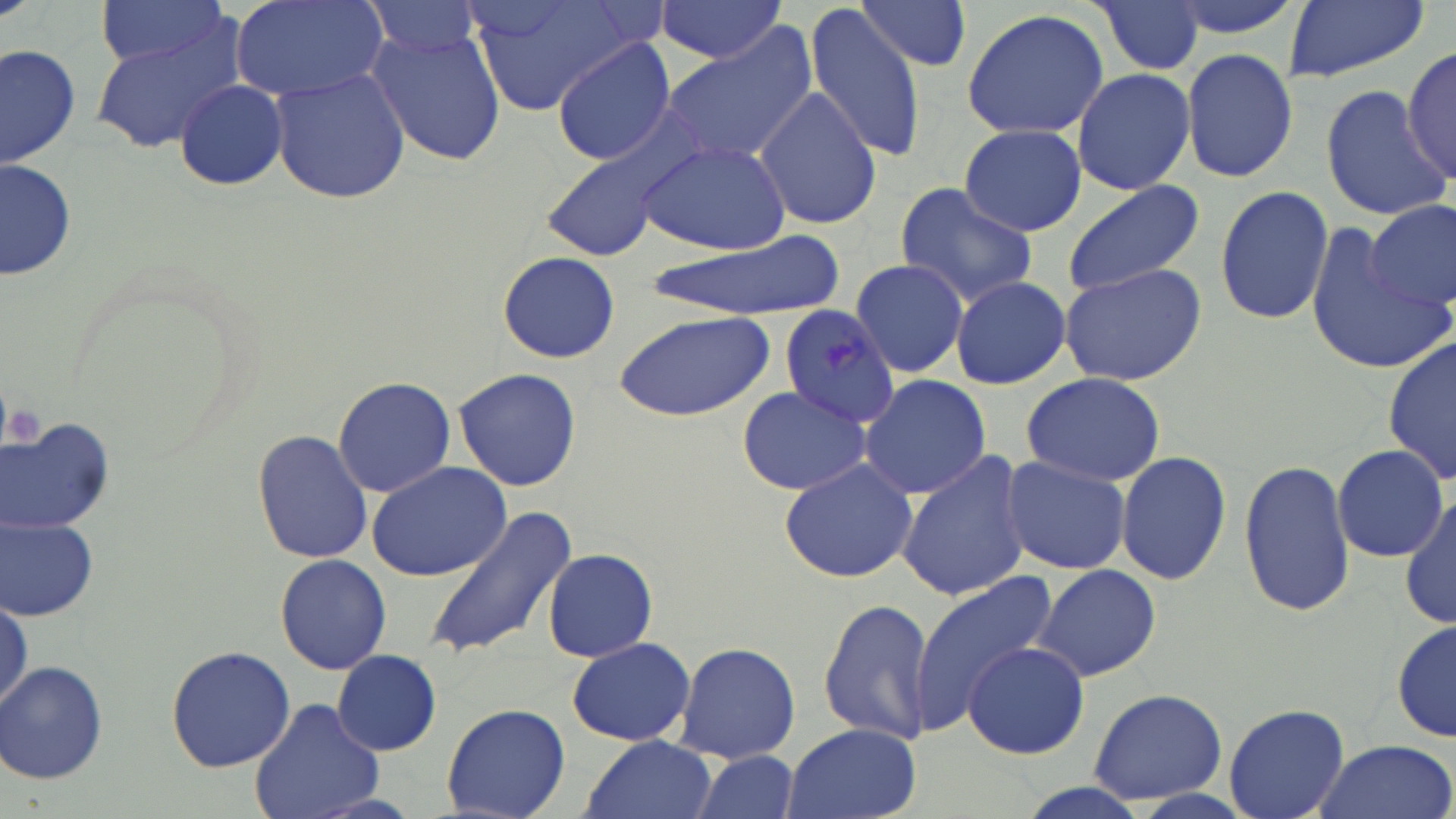 Approximate bounding boxes as (x1, y1, x2, y2) in pixels. Uninfected red blood cell locations: (95, 0, 226, 70), (360, 0, 487, 59), (473, 0, 635, 116), (652, 0, 788, 63), (856, 0, 976, 76), (1279, 0, 1429, 82), (231, 1, 385, 100), (1090, 2, 1204, 77), (804, 7, 924, 164), (958, 8, 1111, 140), (366, 24, 508, 167), (92, 28, 240, 151), (656, 28, 817, 170), (551, 40, 676, 167), (2, 42, 81, 169), (1403, 45, 1456, 187), (1180, 48, 1299, 183), (270, 66, 409, 205), (1071, 66, 1196, 196), (172, 79, 289, 191), (1319, 84, 1448, 221), (753, 85, 881, 233), (959, 123, 1087, 237), (535, 129, 697, 266), (638, 140, 791, 255), (1, 156, 77, 282), (1060, 180, 1205, 296), (894, 182, 1040, 308), (1214, 183, 1334, 327), (1369, 204, 1455, 311), (1303, 223, 1449, 375), (647, 235, 844, 320), (496, 251, 621, 364), (849, 257, 972, 380), (1058, 263, 1207, 387), (949, 275, 1070, 389), (612, 309, 775, 421), (1384, 336, 1456, 487), (452, 368, 585, 494), (1021, 371, 1168, 488), (859, 373, 992, 500), (332, 376, 456, 499), (736, 384, 877, 496), (1, 417, 120, 532), (253, 428, 373, 565), (1333, 444, 1448, 563), (1116, 450, 1233, 585), (895, 452, 1032, 603), (1000, 454, 1132, 574), (778, 458, 919, 583), (1240, 458, 1355, 618), (367, 461, 515, 582), (1400, 491, 1456, 634), (422, 504, 578, 662), (1, 515, 102, 621), (541, 547, 659, 663), (275, 554, 392, 675), (1031, 564, 1162, 682), (911, 572, 1057, 730), (818, 596, 935, 746), (1392, 617, 1456, 746), (567, 636, 695, 746), (673, 640, 801, 762), (964, 642, 1089, 758), (165, 645, 296, 772), (333, 649, 441, 754), (2, 661, 111, 786), (1088, 689, 1226, 806), (250, 698, 384, 819), (442, 702, 571, 819), (1224, 703, 1349, 819), (783, 725, 921, 819), (581, 735, 717, 819), (1309, 738, 1455, 819), (686, 753, 800, 819). Plasmodium malariae-infected red blood cell locations: (778, 304, 904, 431). Platelet locations: (4, 400, 42, 447). Slide-level diagnosis: Plasmodium malariae. Image is 1456×819 pixels. Optical microscopy. Single field of view. May-Grünwald-Giemsa stain. Thin blood film. 1000x magnification.